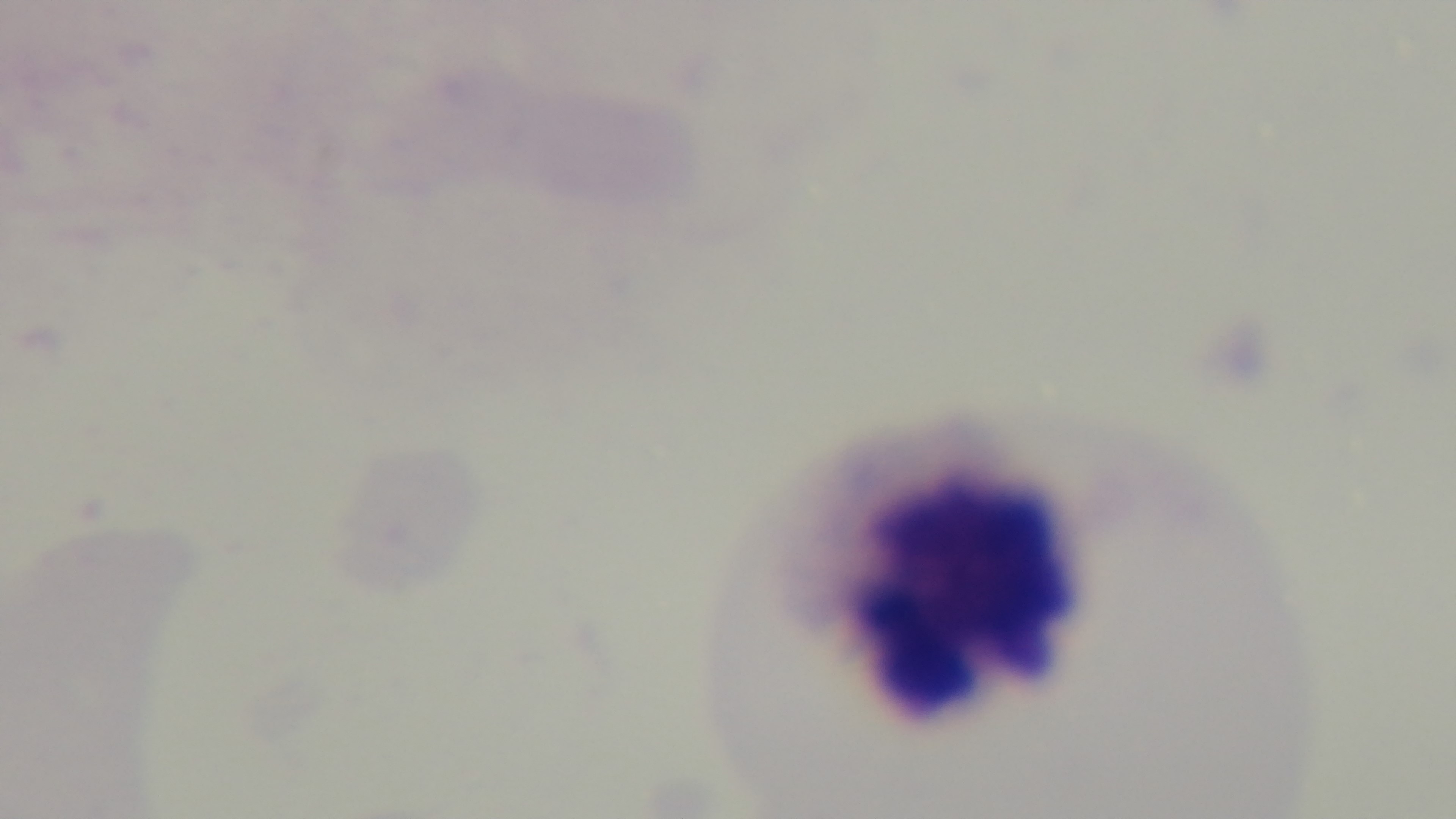
Summary:
  - Preparation: thick smear
  - Malaria status: negative
  - Objective: 100x oil immersion
  - Modality: light microscopy
  - Capture: mounted 4K digital camera
  - Field of view: single
  - Stain: Giemsa